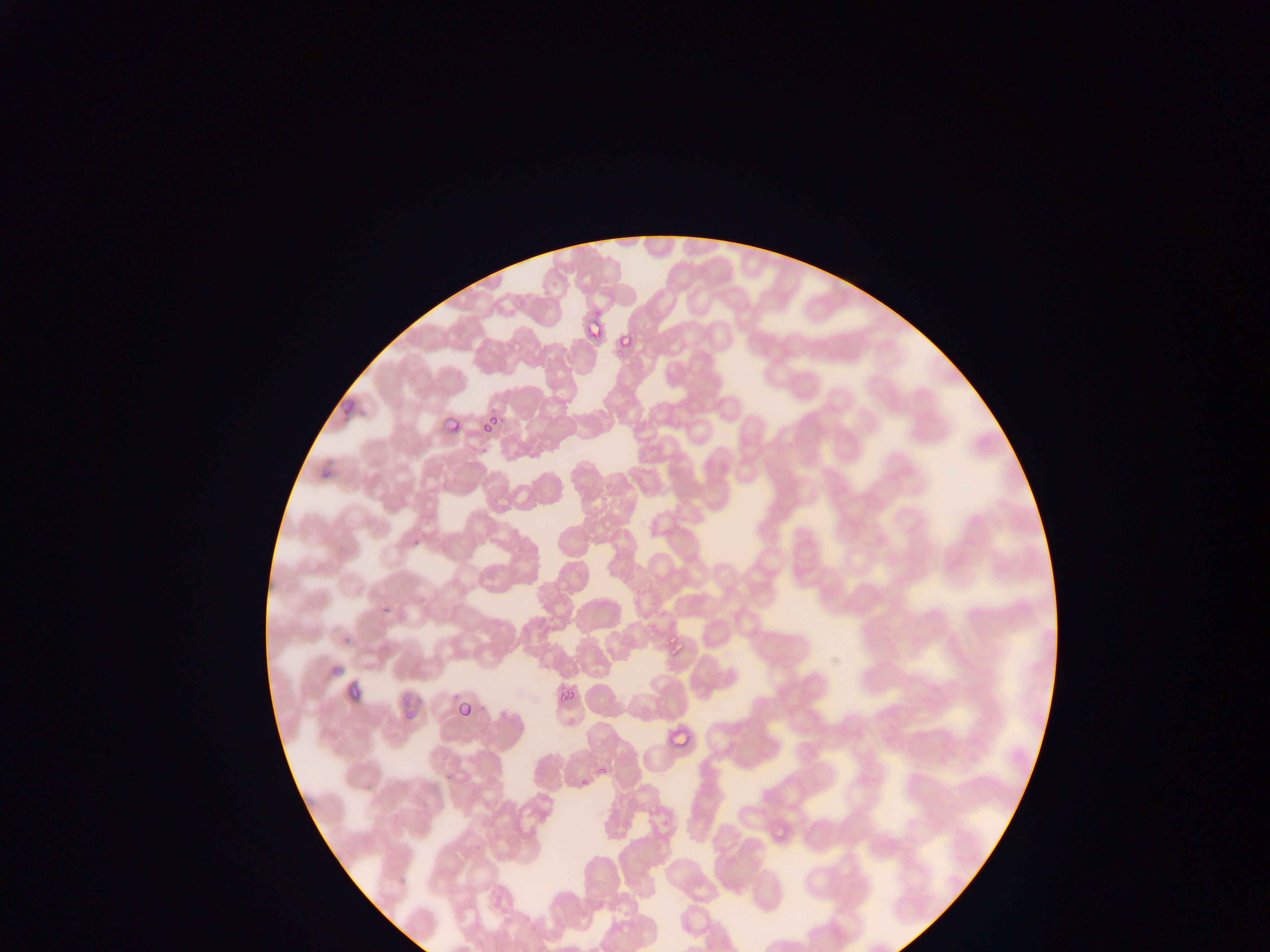

country = Ghana
capture = mobile-phone photograph through a microscope
Plasmodium parasite locations = approximate bounding boxes as (left, top, right, bottom) in pixels: (576, 312, 610, 336), (607, 337, 635, 364), (323, 388, 363, 422), (435, 396, 458, 441), (481, 410, 506, 431), (314, 445, 341, 473), (652, 602, 701, 665), (339, 679, 367, 713), (557, 686, 586, 704), (455, 689, 489, 726), (399, 701, 424, 719), (662, 715, 695, 754), (566, 750, 620, 799), (764, 788, 809, 849)
preparation = thin blood smear
image size = 1270×952 pixels
field of view = single